Name the parasite shown.
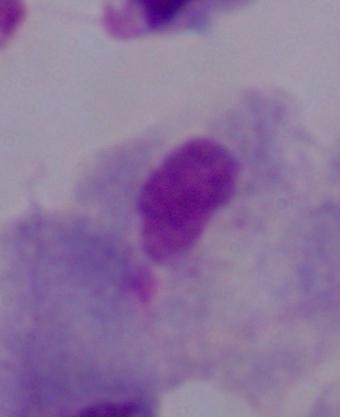

A trichomonad.

Summary:
  - Magnification: 1000x
  - Modality: micrograph